Assess the morphology of the erythrocytes.
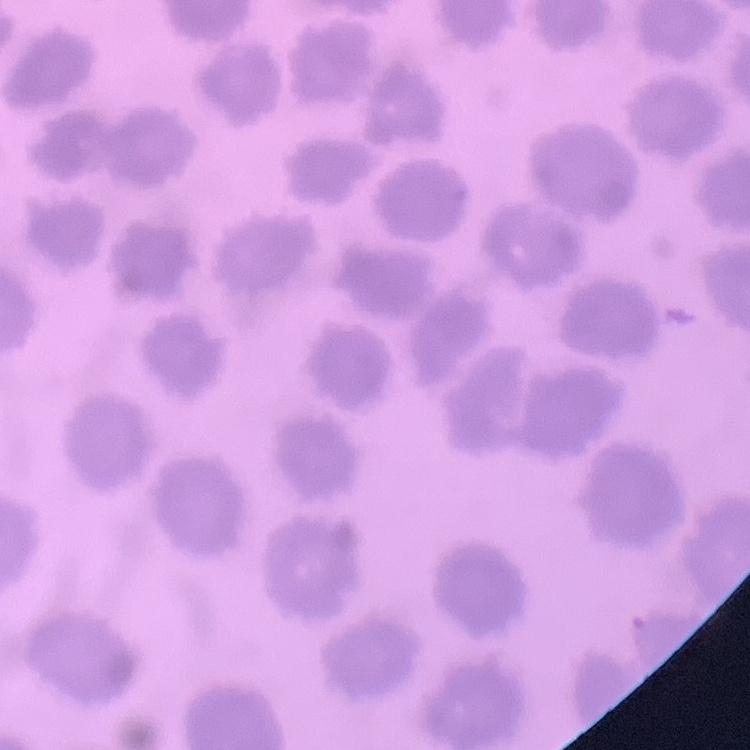
They show no rouleaux formation.

{
  "preparation": "thin blood film",
  "image_type": "square crop of a larger photomicrograph",
  "stain": "Field's or Giemsa"
}